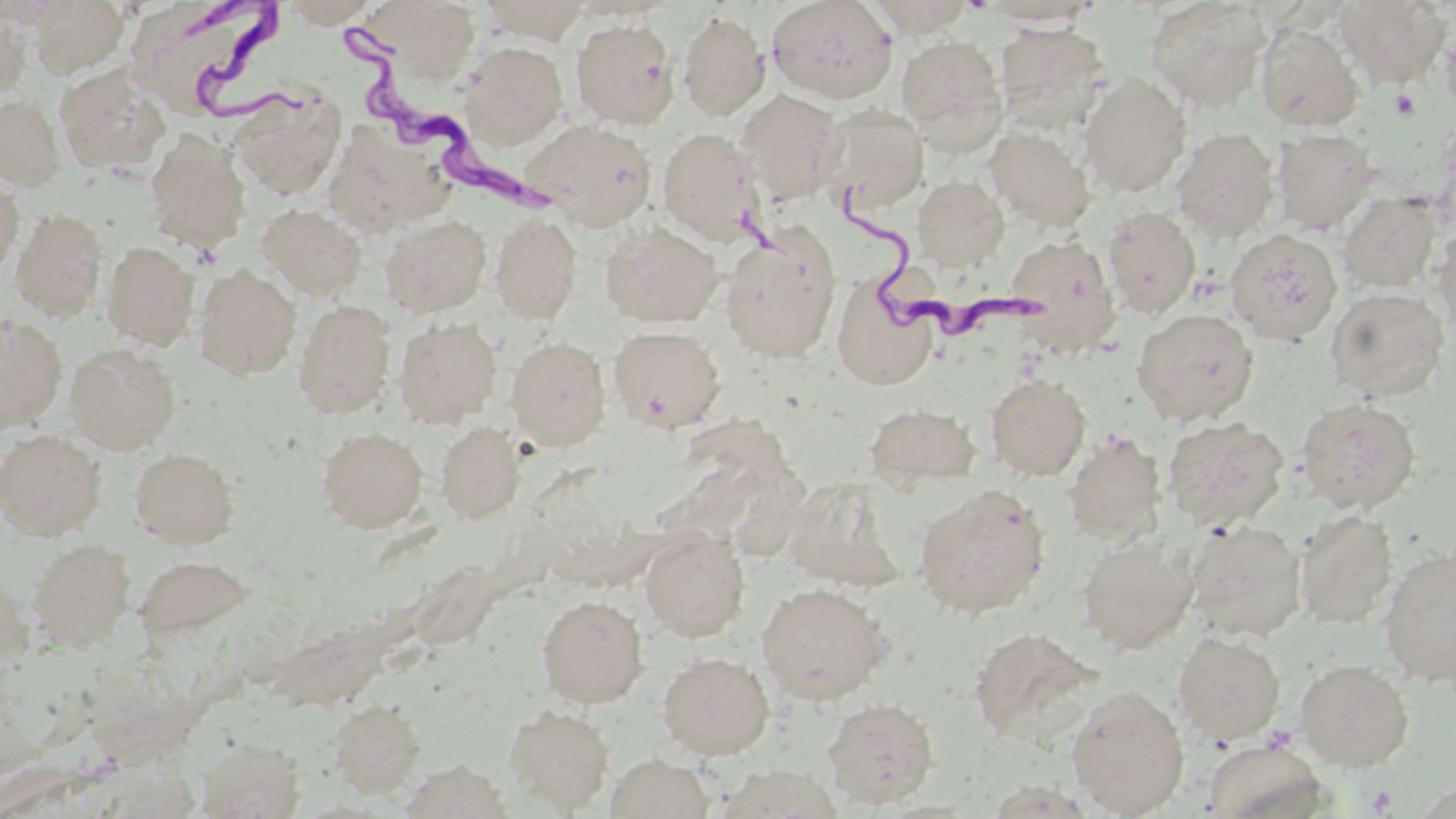
Summary:
  - Coordinate format: approximate bounding boxes as named x1/y1/x2/y2 corners in pixels
  - Platelet locations: (x1=1390, y1=89, x2=1420, y2=120), (x1=1366, y1=784, x2=1397, y2=815)
  - Trypanosoma brucei locations: (x1=189, y1=3, x2=308, y2=127), (x1=331, y1=17, x2=579, y2=220), (x1=846, y1=187, x2=1050, y2=355)
  - Uninfected red blood cell locations: (x1=31, y1=0, x2=129, y2=78), (x1=127, y1=0, x2=290, y2=122), (x1=279, y1=0, x2=380, y2=27), (x1=378, y1=0, x2=482, y2=83), (x1=482, y1=0, x2=590, y2=43), (x1=767, y1=0, x2=898, y2=103), (x1=865, y1=0, x2=975, y2=36), (x1=1336, y1=0, x2=1450, y2=87), (x1=978, y1=1, x2=1102, y2=26), (x1=1146, y1=1, x2=1271, y2=110), (x1=677, y1=10, x2=770, y2=121), (x1=0, y1=12, x2=29, y2=99), (x1=570, y1=19, x2=679, y2=128), (x1=994, y1=22, x2=1111, y2=133), (x1=1256, y1=25, x2=1363, y2=131), (x1=1440, y1=27, x2=1456, y2=122), (x1=896, y1=35, x2=1005, y2=139), (x1=461, y1=43, x2=567, y2=148), (x1=56, y1=66, x2=171, y2=174), (x1=1079, y1=74, x2=1191, y2=197), (x1=232, y1=87, x2=345, y2=199), (x1=736, y1=89, x2=844, y2=203), (x1=0, y1=96, x2=64, y2=190), (x1=1111, y1=101, x2=1232, y2=223), (x1=817, y1=106, x2=929, y2=215), (x1=524, y1=119, x2=657, y2=230), (x1=986, y1=126, x2=1094, y2=231), (x1=323, y1=127, x2=446, y2=235), (x1=1173, y1=127, x2=1279, y2=242), (x1=658, y1=128, x2=762, y2=244), (x1=1273, y1=128, x2=1379, y2=233), (x1=145, y1=130, x2=250, y2=252), (x1=913, y1=176, x2=1008, y2=269), (x1=0, y1=179, x2=22, y2=288), (x1=1338, y1=192, x2=1442, y2=293), (x1=257, y1=204, x2=367, y2=299), (x1=1102, y1=206, x2=1201, y2=318), (x1=11, y1=208, x2=107, y2=321), (x1=381, y1=214, x2=492, y2=317), (x1=490, y1=214, x2=582, y2=324), (x1=600, y1=219, x2=722, y2=328), (x1=1433, y1=220, x2=1456, y2=336), (x1=1225, y1=229, x2=1342, y2=344), (x1=719, y1=231, x2=840, y2=363), (x1=1004, y1=235, x2=1119, y2=353), (x1=102, y1=241, x2=199, y2=349), (x1=194, y1=266, x2=301, y2=379), (x1=834, y1=284, x2=936, y2=388), (x1=1325, y1=288, x2=1449, y2=401), (x1=294, y1=299, x2=396, y2=418), (x1=1133, y1=309, x2=1258, y2=426), (x1=0, y1=314, x2=67, y2=432), (x1=394, y1=317, x2=502, y2=427), (x1=608, y1=325, x2=727, y2=433), (x1=506, y1=336, x2=611, y2=450), (x1=66, y1=343, x2=180, y2=453), (x1=986, y1=373, x2=1091, y2=480), (x1=1296, y1=397, x2=1421, y2=513), (x1=864, y1=403, x2=980, y2=490), (x1=1162, y1=416, x2=1289, y2=530), (x1=436, y1=422, x2=522, y2=523), (x1=317, y1=427, x2=427, y2=532), (x1=0, y1=430, x2=105, y2=541), (x1=1062, y1=431, x2=1167, y2=543), (x1=129, y1=447, x2=240, y2=549), (x1=778, y1=476, x2=905, y2=590), (x1=913, y1=483, x2=1049, y2=617), (x1=1294, y1=510, x2=1398, y2=629), (x1=1186, y1=519, x2=1307, y2=640), (x1=640, y1=527, x2=750, y2=642), (x1=1077, y1=536, x2=1198, y2=654), (x1=27, y1=538, x2=135, y2=651), (x1=1379, y1=548, x2=1456, y2=686), (x1=135, y1=553, x2=251, y2=645), (x1=0, y1=575, x2=32, y2=674), (x1=756, y1=581, x2=890, y2=705), (x1=537, y1=595, x2=648, y2=705), (x1=969, y1=627, x2=1098, y2=744), (x1=1174, y1=632, x2=1285, y2=743), (x1=657, y1=651, x2=774, y2=758), (x1=1295, y1=658, x2=1413, y2=771), (x1=1066, y1=685, x2=1190, y2=817), (x1=822, y1=697, x2=939, y2=808), (x1=328, y1=698, x2=425, y2=797), (x1=505, y1=704, x2=614, y2=813), (x1=197, y1=737, x2=305, y2=817), (x1=1203, y1=739, x2=1328, y2=819), (x1=606, y1=752, x2=714, y2=818), (x1=713, y1=765, x2=846, y2=819)
  - Slide-level diagnosis: Trypanosoma brucei
  - Image size: 1456×819 pixels
  - Magnification: 1000x
  - Preparation: thin blood film
  - Modality: light microscopy
  - Field of view: single
  - Stain: May-Grünwald-Giemsa